Look for Plasmodium parasites.
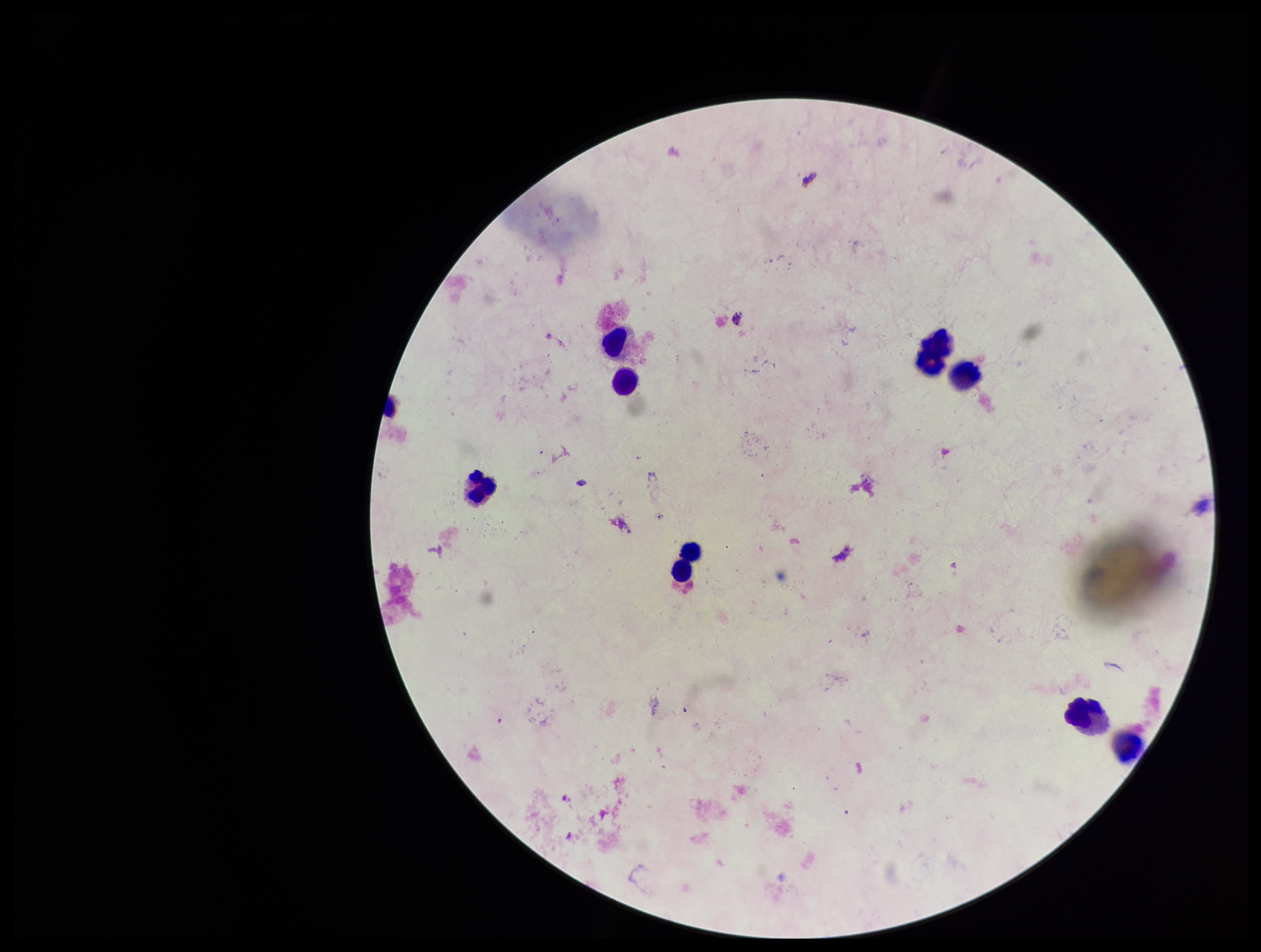

None detected.

capture = smartphone photograph through the microscope eyepiece
preparation = thick
stain = Giemsa
leukocyte count = 8
parasite count = 0
field of view = single
image size = 1261×952 pixels
patient malaria status = negative